Give the extent of all uninfected red blood cells.
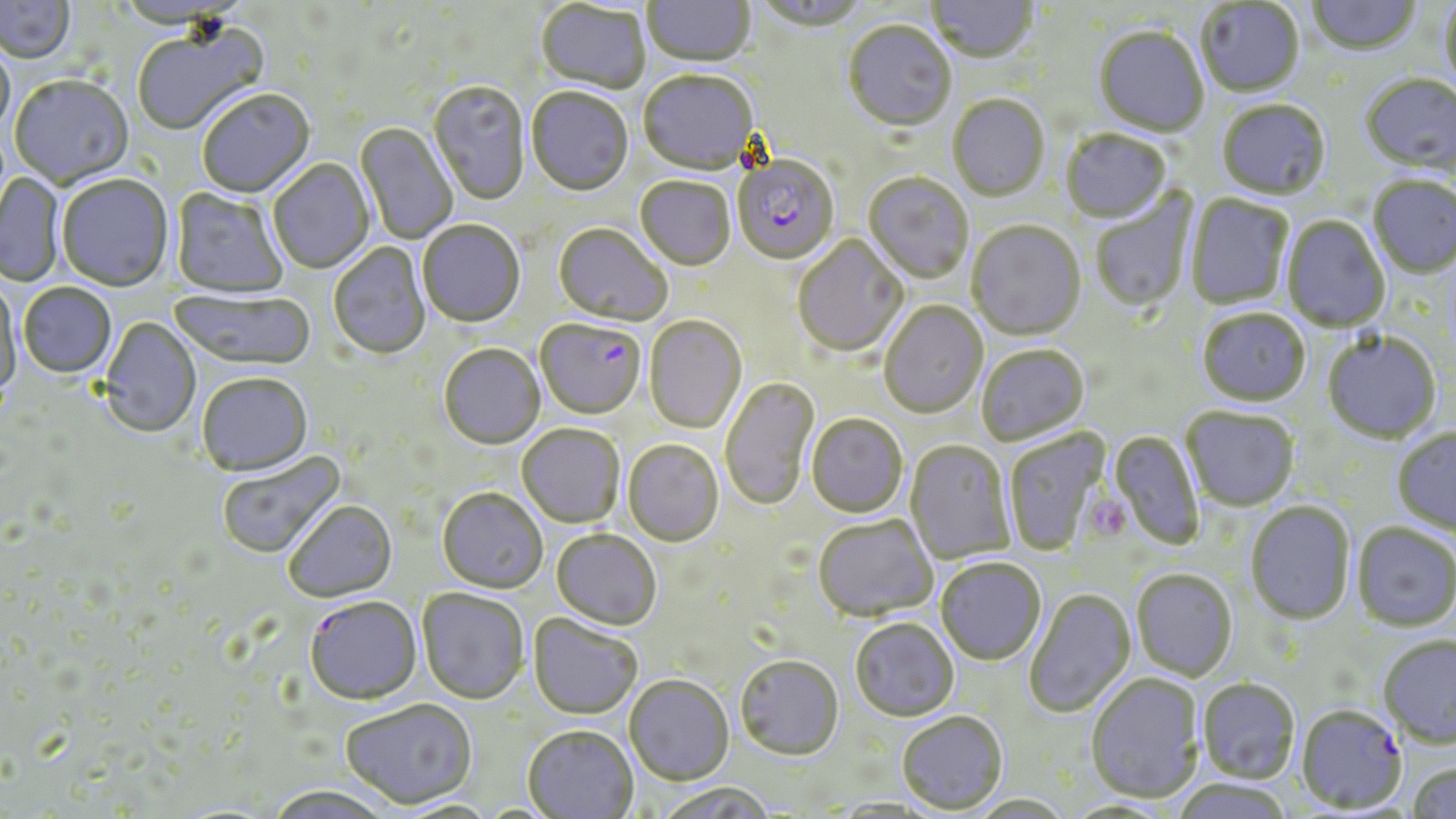

Approximate bounding boxes as (x1,y1)-(x2,y2) corner pairs in pixels.
Uninfected red blood cells: (0,0)-(75,65), (643,0)-(755,69), (752,0)-(872,34), (1307,0)-(1421,58), (926,1)-(1039,66), (1196,1)-(1304,99), (535,2)-(650,96), (1439,2)-(1456,97), (843,22)-(956,133), (133,24)-(270,138), (1094,28)-(1209,139), (0,39)-(14,144), (638,72)-(759,177), (1360,75)-(1456,178), (10,77)-(134,190), (428,82)-(530,206), (527,89)-(633,198), (197,90)-(316,200), (947,96)-(1049,202), (1217,101)-(1331,201), (355,123)-(457,244), (1060,130)-(1172,225), (268,159)-(375,275), (0,172)-(65,287), (863,173)-(973,284), (57,176)-(174,293), (1367,176)-(1456,279), (635,178)-(736,272), (1089,188)-(1198,314), (170,189)-(288,299), (1186,194)-(1294,310), (1281,216)-(1390,333), (418,221)-(526,328), (967,221)-(1086,342), (553,224)-(672,327), (792,235)-(907,357), (328,243)-(431,361), (1,281)-(22,404), (18,284)-(117,380), (168,289)-(316,373), (880,301)-(988,419), (1197,309)-(1311,407), (644,316)-(747,434), (100,318)-(202,438), (1322,331)-(1441,443), (439,345)-(545,450), (976,345)-(1089,446), (196,374)-(313,478), (720,377)-(820,511), (1181,406)-(1300,511), (806,415)-(908,518), (517,425)-(624,528), (1392,428)-(1456,536), (1003,429)-(1112,557), (1110,430)-(1204,550), (622,440)-(723,547), (906,441)-(1015,564), (217,451)-(346,560), (437,490)-(548,595), (1245,501)-(1355,624), (284,502)-(398,604), (813,515)-(938,622), (1352,522)-(1456,631), (552,530)-(661,631), (935,558)-(1045,665), (1132,568)-(1238,681), (1025,588)-(1135,718), (417,589)-(529,705), (305,598)-(422,707), (528,614)-(643,720), (850,618)-(959,722), (1378,634)-(1456,747), (735,655)-(844,761), (1086,673)-(1205,803), (625,676)-(733,786), (1197,677)-(1300,783), (341,700)-(478,810), (897,712)-(1008,815), (522,726)-(638,818), (1408,760)-(1456,819), (1170,778)-(1295,819), (654,782)-(778,819), (264,785)-(394,818), (967,794)-(1076,818).

Platelet locations: (1085,498)-(1130,541). Plasmodium falciparum-infected red blood cell locations: (733,157)-(839,266), (535,320)-(645,420), (1296,704)-(1407,813). Slide-level diagnosis: Plasmodium falciparum. Image is 1456×819 pixels. Single field of view. Optical microscopy. Thin blood film. 1000x magnification. May-Grünwald-Giemsa-stained preparation.